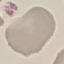
Summary:
  - Result: no malaria parasites detected
  - Stain: Giemsa
  - Image type: cell patch, automatically extracted from a larger field of view and resized to 64 × 64 pixels
  - Capture: smartphone camera at the microscope eyepiece
  - Preparation: thin blood smear